Locate every Plasmodium falciparum-infected red blood cell.
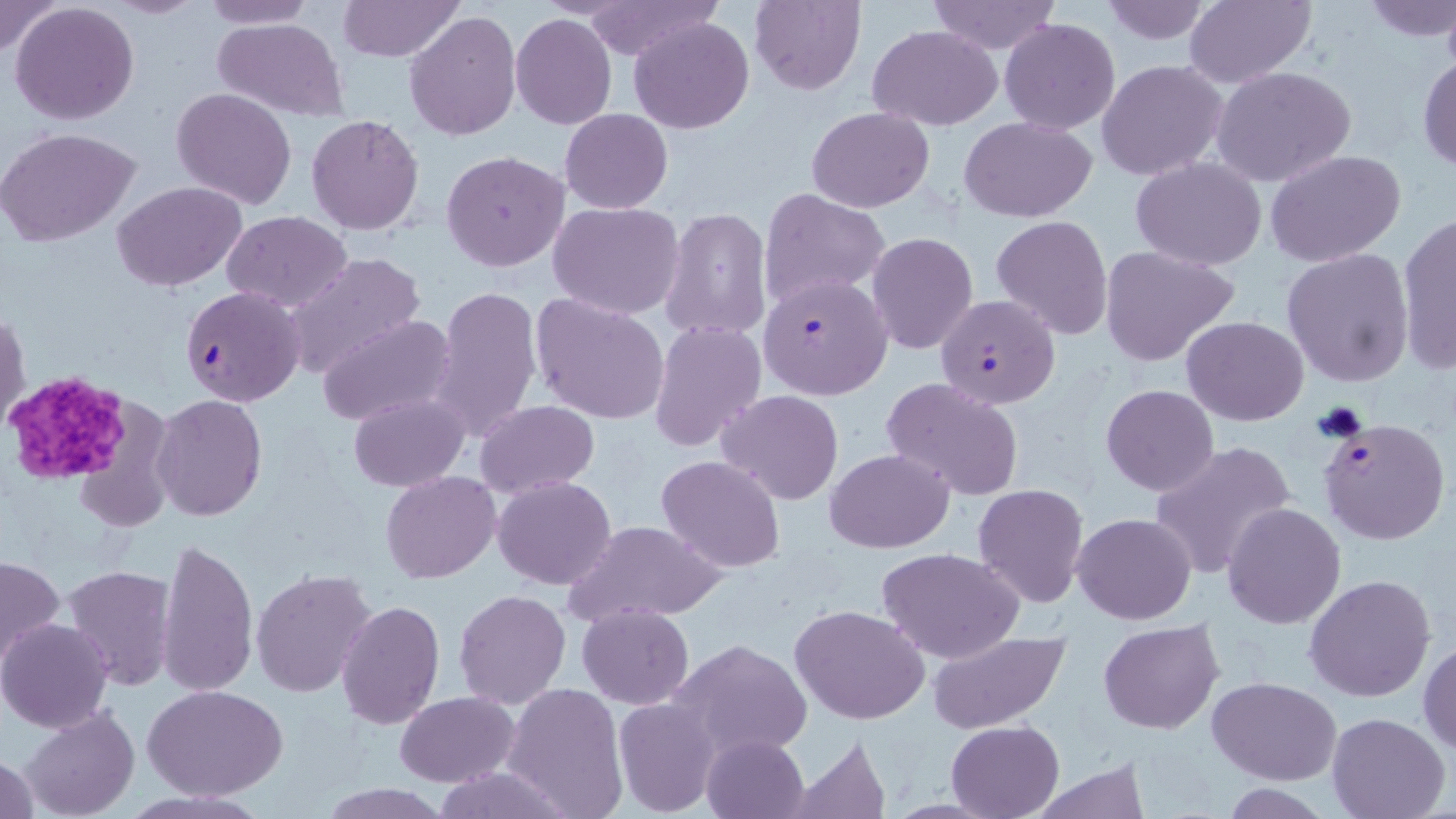

Approximate bounding boxes as [x1, y1, x2, y2] in pixels.
Plasmodium falciparum-infected red blood cells: [757, 273, 893, 400], [180, 286, 307, 407], [935, 293, 1060, 409], [1318, 417, 1449, 545].

Platelet locations: [3, 372, 132, 486]. Uninfected red blood cell locations: [0, 0, 62, 57], [105, 0, 209, 19], [201, 0, 314, 28], [337, 0, 465, 61], [748, 0, 866, 95], [927, 0, 1061, 54], [1099, 0, 1215, 46], [1182, 0, 1316, 88], [1360, 0, 1456, 41], [576, 1, 719, 62], [10, 2, 141, 125], [404, 11, 521, 141], [510, 13, 618, 129], [213, 16, 348, 120], [628, 16, 753, 134], [999, 18, 1121, 134], [868, 26, 1003, 128], [1417, 50, 1455, 175], [1097, 59, 1229, 182], [1212, 66, 1357, 188], [171, 87, 297, 209], [807, 106, 934, 211], [560, 108, 673, 213], [306, 115, 425, 235], [959, 117, 1098, 220], [0, 127, 140, 247], [1264, 149, 1406, 266], [441, 151, 571, 272], [1131, 157, 1268, 269], [112, 182, 248, 291], [759, 188, 892, 307], [547, 200, 685, 319], [663, 208, 771, 342], [221, 210, 351, 311], [1396, 213, 1456, 373], [991, 215, 1114, 341], [867, 232, 978, 355], [1099, 244, 1240, 367], [1282, 248, 1415, 386], [279, 251, 425, 377], [427, 284, 541, 445], [533, 294, 670, 425], [1, 309, 29, 431], [316, 314, 458, 427], [1183, 316, 1309, 423], [650, 320, 767, 450], [880, 377, 1026, 501], [1101, 385, 1218, 496], [717, 389, 844, 505], [152, 394, 266, 520], [348, 394, 468, 490], [1125, 398, 1261, 552], [475, 402, 599, 498], [1151, 440, 1297, 580], [826, 448, 954, 554], [656, 456, 785, 572], [486, 471, 606, 698], [380, 472, 500, 584], [493, 476, 618, 589], [973, 482, 1090, 607], [1222, 502, 1346, 627], [1072, 513, 1196, 624], [562, 519, 727, 624], [157, 536, 258, 696], [876, 547, 1027, 664], [1, 555, 65, 666], [63, 564, 177, 691], [250, 569, 376, 696], [1305, 573, 1436, 703], [454, 589, 570, 709], [336, 599, 444, 730], [576, 603, 695, 708], [790, 604, 932, 724], [1, 618, 115, 734], [1098, 620, 1224, 735], [927, 629, 1070, 734], [667, 637, 813, 764], [1419, 640, 1456, 756], [1208, 677, 1342, 784], [144, 683, 289, 800], [502, 683, 629, 818], [394, 692, 518, 786], [614, 697, 721, 817], [21, 707, 140, 819], [1326, 712, 1451, 819], [948, 720, 1064, 818], [700, 733, 810, 819], [787, 735, 895, 817], [1, 752, 42, 818], [1028, 761, 1152, 818], [427, 767, 570, 818], [315, 783, 453, 818], [120, 789, 268, 819]. Slide-level diagnosis: Plasmodium falciparum. May-Grünwald-Giemsa stain. Optical microscopy. Captured at 1000x magnification. Thin blood smear. One field of a larger specimen. Image is 1456×819 pixels.